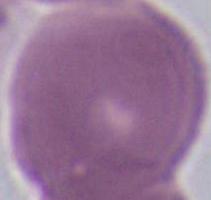
1000x magnification. Photomicrograph. A red blood cell is seen.